Identify the blood parasite species.
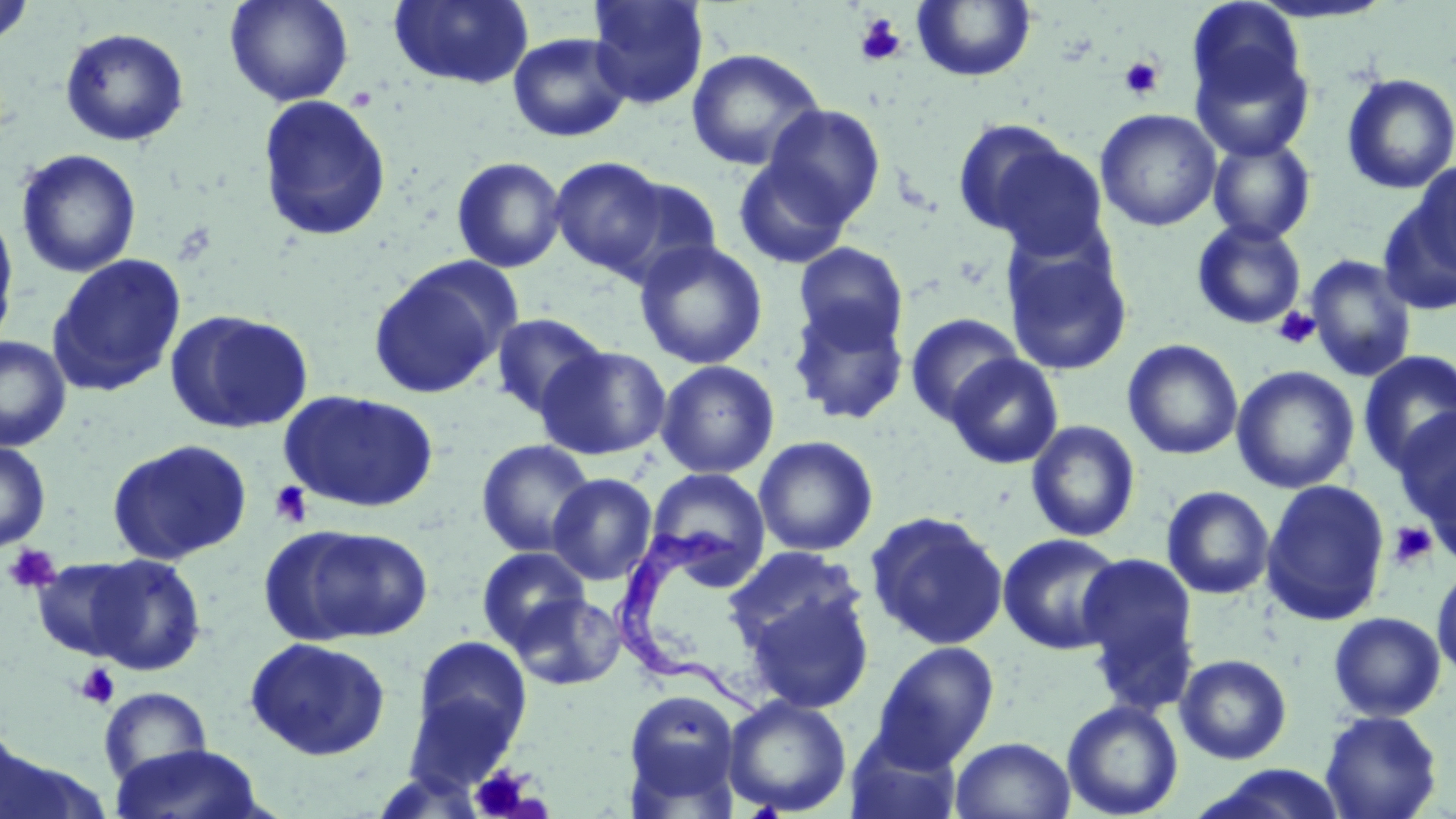

Trypanosoma brucei.

modality: optical microscopy
trypanosoma_brucei_locations: 'approximate bounding boxes as (x1,y1)-(x2,y2) corner pairs in pixels: (606,525)-(771,719)'
field_of_view: one of a larger specimen
magnification: 1000x
stain: May-Grünwald-Giemsa
preparation: thin blood film
image_size: 1456×819 pixels
uninfected_red_blood_cell_locations: 'approximate bounding boxes as (x1,y1)-(x2,y2) corner pairs in pixels: (224,0)-(354,107), (389,0)-(535,89), (587,0)-(709,109), (1187,0)-(1306,114), (912,1)-(1036,83), (1245,1)-(1395,24), (1,2)-(36,48), (59,27)-(189,146), (507,32)-(632,142), (1189,38)-(1316,162), (686,48)-(826,171), (1340,72)-(1455,195), (256,94)-(392,242), (763,104)-(886,225), (1095,108)-(1221,232), (967,130)-(1109,260), (1207,137)-(1316,244), (15,149)-(142,278), (451,156)-(567,272), (549,156)-(669,276), (733,157)-(854,270), (1410,159)-(1456,283), (605,176)-(724,286), (1378,196)-(1456,316), (0,207)-(19,348), (1191,220)-(1307,330), (1001,237)-(1135,377), (635,239)-(768,370), (793,241)-(909,351), (48,254)-(187,396), (1302,254)-(1418,382), (369,256)-(519,398), (786,297)-(910,425), (165,309)-(312,435), (490,312)-(608,420), (905,313)-(1024,424), (0,335)-(72,452), (1122,339)-(1244,460), (535,345)-(671,461), (1357,350)-(1456,474), (947,353)-(1064,469), (655,360)-(779,479), (1231,365)-(1359,494), (279,390)-(439,513), (1392,408)-(1456,530), (1025,420)-(1141,542), (753,435)-(878,556), (476,439)-(596,558), (107,440)-(252,565), (0,441)-(51,552), (1421,444)-(1455,570), (646,468)-(770,587), (548,473)-(657,585), (1260,478)-(1391,626), (1161,486)-(1275,599), (865,510)-(1009,650), (277,524)-(434,644), (998,533)-(1125,654), (723,545)-(866,657), (477,547)-(591,652), (1076,552)-(1201,704), (80,553)-(207,675), (30,557)-(147,661), (1431,562)-(1456,683), (742,587)-(875,715), (509,591)-(625,691), (1328,611)-(1447,722), (410,634)-(533,775), (244,637)-(391,761), (873,642)-(999,768), (1174,654)-(1292,765), (99,687)-(213,785), (622,688)-(742,812), (723,694)-(852,816), (1061,699)-(1184,818), (1320,709)-(1443,819), (0,720)-(50,819), (845,730)-(963,819), (949,736)-(1076,818), (0,737)-(104,818), (109,743)-(267,819), (1195,765)-(1350,819)'
platelet_locations: 'approximate bounding boxes as (x1,y1)-(x2,y2) corner pairs in pixels: (854,13)-(907,67), (1118,56)-(1164,100), (1272,306)-(1320,349), (269,481)-(312,527), (1388,521)-(1437,570), (3,544)-(62,594), (75,663)-(120,709), (469,766)-(542,817)'